State which parasite is depicted.
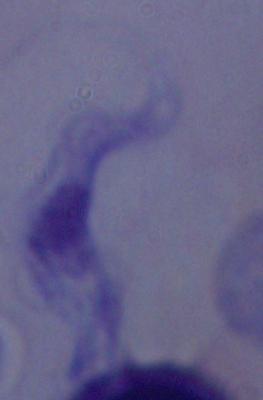
A trypanosome.

magnification = 1000x
modality = photomicrograph